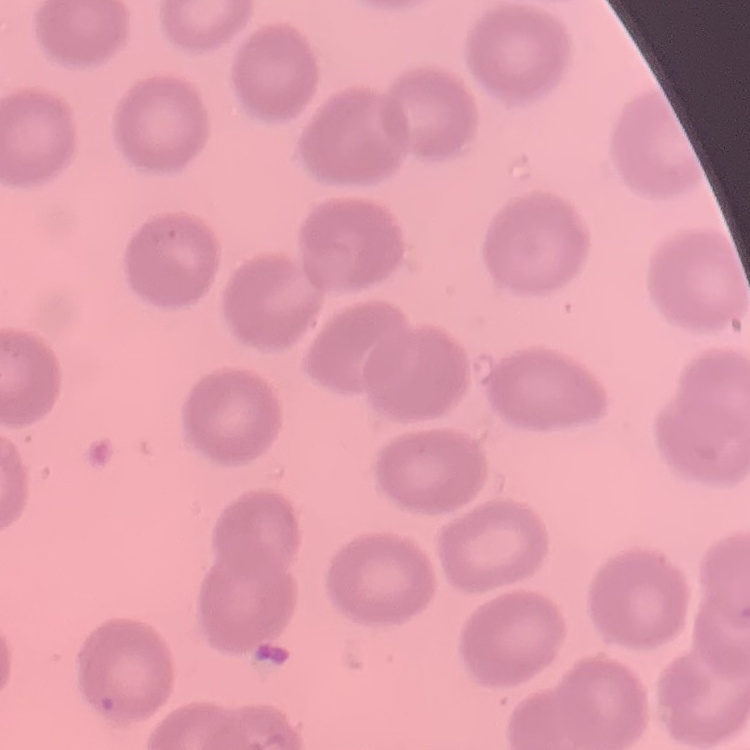

Summary:
  - Red blood cell morphology: no rouleaux formation
  - Image type: square crop of a larger photomicrograph
  - Stain: Field's or Giemsa
  - Preparation: thin blood smear